Locate and identify every blood parasite.
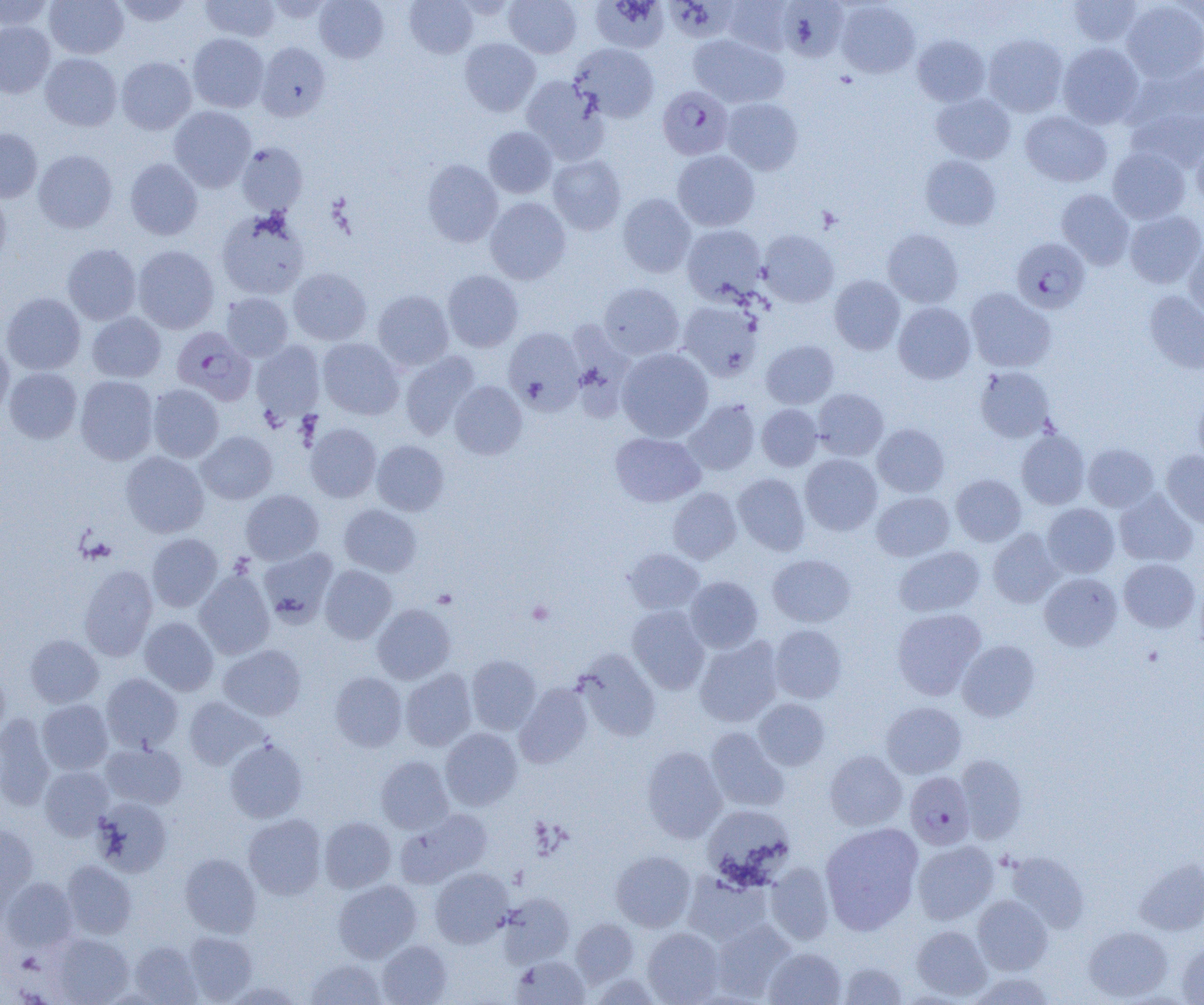
Approximate bounding boxes as named x1/y1/x2/y2 corners in pixels.
Plasmodium falciparum-infected red blood cells: (x1=658, y1=86, x2=734, y2=160), (x1=1012, y1=238, x2=1090, y2=313), (x1=172, y1=327, x2=255, y2=405), (x1=905, y1=771, x2=975, y2=850).
No Plasmodium ovale, Plasmodium malariae, Plasmodium vivax, Babesia divergens, or Trypanosoma brucei observed.

slide-level diagnosis = Plasmodium falciparum
image size = 1204×1005 pixels
modality = light microscopy
platelet locations = approximate bounding boxes as named x1/y1/x2/y2 corners in pixels: (x1=527, y1=600, x2=555, y2=625)
magnification = 1000x
preparation = thin blood smear
uninfected red blood cell locations = approximate bounding boxes as named x1/y1/x2/y2 corners in pixels: (x1=45, y1=0, x2=129, y2=59), (x1=113, y1=0, x2=194, y2=27), (x1=199, y1=0, x2=280, y2=41), (x1=314, y1=0, x2=389, y2=63), (x1=404, y1=0, x2=478, y2=58), (x1=504, y1=0, x2=582, y2=58), (x1=590, y1=0, x2=669, y2=53), (x1=778, y1=0, x2=847, y2=62), (x1=0, y1=1, x2=54, y2=30), (x1=723, y1=1, x2=795, y2=55), (x1=836, y1=1, x2=920, y2=78), (x1=1067, y1=1, x2=1145, y2=46), (x1=1121, y1=1, x2=1204, y2=82), (x1=0, y1=21, x2=55, y2=98), (x1=188, y1=33, x2=268, y2=112), (x1=688, y1=34, x2=788, y2=108), (x1=983, y1=34, x2=1068, y2=117), (x1=912, y1=35, x2=990, y2=107), (x1=459, y1=37, x2=541, y2=116), (x1=256, y1=41, x2=331, y2=121), (x1=570, y1=43, x2=659, y2=122), (x1=1058, y1=43, x2=1144, y2=129), (x1=40, y1=53, x2=122, y2=131), (x1=116, y1=57, x2=197, y2=134), (x1=1126, y1=61, x2=1204, y2=132), (x1=521, y1=75, x2=609, y2=163), (x1=931, y1=92, x2=1016, y2=164), (x1=722, y1=97, x2=803, y2=174), (x1=169, y1=106, x2=256, y2=191), (x1=1127, y1=106, x2=1204, y2=173), (x1=1019, y1=110, x2=1112, y2=187), (x1=483, y1=127, x2=557, y2=198), (x1=0, y1=129, x2=42, y2=202), (x1=1191, y1=138, x2=1204, y2=210), (x1=236, y1=142, x2=307, y2=215), (x1=1108, y1=147, x2=1190, y2=224), (x1=33, y1=150, x2=118, y2=233), (x1=672, y1=150, x2=760, y2=231), (x1=547, y1=154, x2=626, y2=235), (x1=920, y1=155, x2=1001, y2=231), (x1=125, y1=158, x2=203, y2=240), (x1=422, y1=159, x2=503, y2=247), (x1=0, y1=188, x2=11, y2=268), (x1=1057, y1=189, x2=1135, y2=269), (x1=617, y1=193, x2=696, y2=277), (x1=485, y1=197, x2=571, y2=284), (x1=216, y1=210, x2=310, y2=300), (x1=1124, y1=210, x2=1204, y2=288), (x1=682, y1=224, x2=766, y2=304), (x1=882, y1=228, x2=964, y2=308), (x1=758, y1=229, x2=839, y2=307), (x1=1184, y1=241, x2=1204, y2=325), (x1=62, y1=244, x2=142, y2=325), (x1=133, y1=245, x2=220, y2=333), (x1=288, y1=268, x2=372, y2=345), (x1=442, y1=270, x2=524, y2=352), (x1=829, y1=275, x2=905, y2=355), (x1=598, y1=282, x2=684, y2=360), (x1=965, y1=287, x2=1056, y2=373), (x1=372, y1=290, x2=454, y2=371), (x1=1144, y1=290, x2=1204, y2=374), (x1=1, y1=292, x2=85, y2=375), (x1=221, y1=292, x2=293, y2=361), (x1=677, y1=299, x2=764, y2=382), (x1=893, y1=302, x2=976, y2=384), (x1=87, y1=312, x2=166, y2=382), (x1=503, y1=327, x2=585, y2=414), (x1=318, y1=338, x2=404, y2=420), (x1=0, y1=339, x2=14, y2=418), (x1=251, y1=340, x2=325, y2=421), (x1=761, y1=340, x2=839, y2=409), (x1=617, y1=347, x2=714, y2=442), (x1=399, y1=351, x2=480, y2=439), (x1=975, y1=366, x2=1055, y2=443), (x1=4, y1=367, x2=82, y2=443), (x1=75, y1=376, x2=158, y2=464), (x1=450, y1=381, x2=527, y2=459), (x1=148, y1=384, x2=223, y2=462), (x1=813, y1=388, x2=889, y2=460), (x1=1193, y1=392, x2=1204, y2=467), (x1=685, y1=399, x2=760, y2=476), (x1=757, y1=404, x2=822, y2=471), (x1=305, y1=422, x2=381, y2=502), (x1=872, y1=423, x2=950, y2=497), (x1=1016, y1=429, x2=1090, y2=509), (x1=197, y1=431, x2=277, y2=504), (x1=610, y1=432, x2=705, y2=507), (x1=372, y1=440, x2=449, y2=515), (x1=1083, y1=443, x2=1158, y2=511), (x1=1161, y1=450, x2=1204, y2=529), (x1=121, y1=451, x2=209, y2=537), (x1=800, y1=454, x2=882, y2=535), (x1=733, y1=473, x2=810, y2=555), (x1=951, y1=474, x2=1026, y2=546), (x1=668, y1=488, x2=741, y2=563), (x1=1114, y1=489, x2=1198, y2=567), (x1=241, y1=490, x2=324, y2=564), (x1=872, y1=491, x2=954, y2=561), (x1=1042, y1=503, x2=1119, y2=578), (x1=339, y1=504, x2=421, y2=577), (x1=988, y1=529, x2=1063, y2=607), (x1=147, y1=533, x2=223, y2=611), (x1=893, y1=546, x2=985, y2=617), (x1=258, y1=547, x2=337, y2=626), (x1=623, y1=548, x2=705, y2=615), (x1=767, y1=554, x2=855, y2=627), (x1=1118, y1=558, x2=1200, y2=633), (x1=79, y1=564, x2=158, y2=661), (x1=320, y1=565, x2=397, y2=643), (x1=195, y1=570, x2=274, y2=659), (x1=1039, y1=572, x2=1122, y2=651), (x1=685, y1=576, x2=763, y2=653), (x1=372, y1=603, x2=456, y2=684), (x1=627, y1=606, x2=710, y2=694), (x1=891, y1=608, x2=986, y2=700), (x1=140, y1=617, x2=219, y2=695), (x1=769, y1=624, x2=847, y2=703), (x1=25, y1=634, x2=103, y2=707), (x1=694, y1=637, x2=783, y2=727), (x1=958, y1=640, x2=1040, y2=721), (x1=217, y1=644, x2=306, y2=721), (x1=575, y1=650, x2=661, y2=742), (x1=466, y1=655, x2=541, y2=734), (x1=0, y1=667, x2=10, y2=738), (x1=401, y1=669, x2=476, y2=751), (x1=330, y1=672, x2=407, y2=752), (x1=101, y1=673, x2=183, y2=752), (x1=514, y1=682, x2=593, y2=768), (x1=184, y1=696, x2=269, y2=770), (x1=753, y1=698, x2=830, y2=770), (x1=37, y1=699, x2=113, y2=774), (x1=881, y1=702, x2=966, y2=778), (x1=0, y1=713, x2=56, y2=811), (x1=706, y1=727, x2=788, y2=811), (x1=440, y1=728, x2=523, y2=810), (x1=225, y1=739, x2=307, y2=823), (x1=101, y1=740, x2=187, y2=809), (x1=642, y1=746, x2=727, y2=842), (x1=824, y1=751, x2=907, y2=830), (x1=955, y1=754, x2=1028, y2=843), (x1=376, y1=755, x2=454, y2=834), (x1=40, y1=766, x2=113, y2=839), (x1=93, y1=797, x2=172, y2=877), (x1=702, y1=804, x2=795, y2=885), (x1=395, y1=809, x2=493, y2=888), (x1=243, y1=814, x2=326, y2=899), (x1=319, y1=816, x2=396, y2=893), (x1=820, y1=822, x2=923, y2=935), (x1=0, y1=824, x2=38, y2=914), (x1=912, y1=840, x2=999, y2=924), (x1=611, y1=850, x2=696, y2=932), (x1=1003, y1=851, x2=1089, y2=931), (x1=180, y1=853, x2=261, y2=938), (x1=1135, y1=858, x2=1204, y2=935), (x1=62, y1=860, x2=136, y2=938), (x1=764, y1=862, x2=834, y2=944), (x1=430, y1=867, x2=513, y2=947), (x1=682, y1=871, x2=772, y2=945), (x1=2, y1=877, x2=78, y2=951), (x1=333, y1=879, x2=422, y2=963), (x1=498, y1=892, x2=575, y2=967), (x1=972, y1=895, x2=1053, y2=975), (x1=571, y1=919, x2=639, y2=987), (x1=711, y1=919, x2=795, y2=999), (x1=911, y1=925, x2=992, y2=1000), (x1=1083, y1=925, x2=1173, y2=1001), (x1=642, y1=927, x2=725, y2=1004), (x1=183, y1=931, x2=257, y2=1003), (x1=51, y1=933, x2=132, y2=1004), (x1=377, y1=939, x2=452, y2=1005), (x1=129, y1=941, x2=201, y2=1004), (x1=1176, y1=941, x2=1204, y2=1004), (x1=764, y1=947, x2=846, y2=1005), (x1=510, y1=954, x2=590, y2=1004), (x1=305, y1=958, x2=387, y2=1004), (x1=838, y1=961, x2=908, y2=1004), (x1=967, y1=971, x2=1057, y2=1004), (x1=221, y1=981, x2=302, y2=1005)
field of view = one of a larger specimen